Give the extent of all Plasmodium falciparum-infected red blood cells.
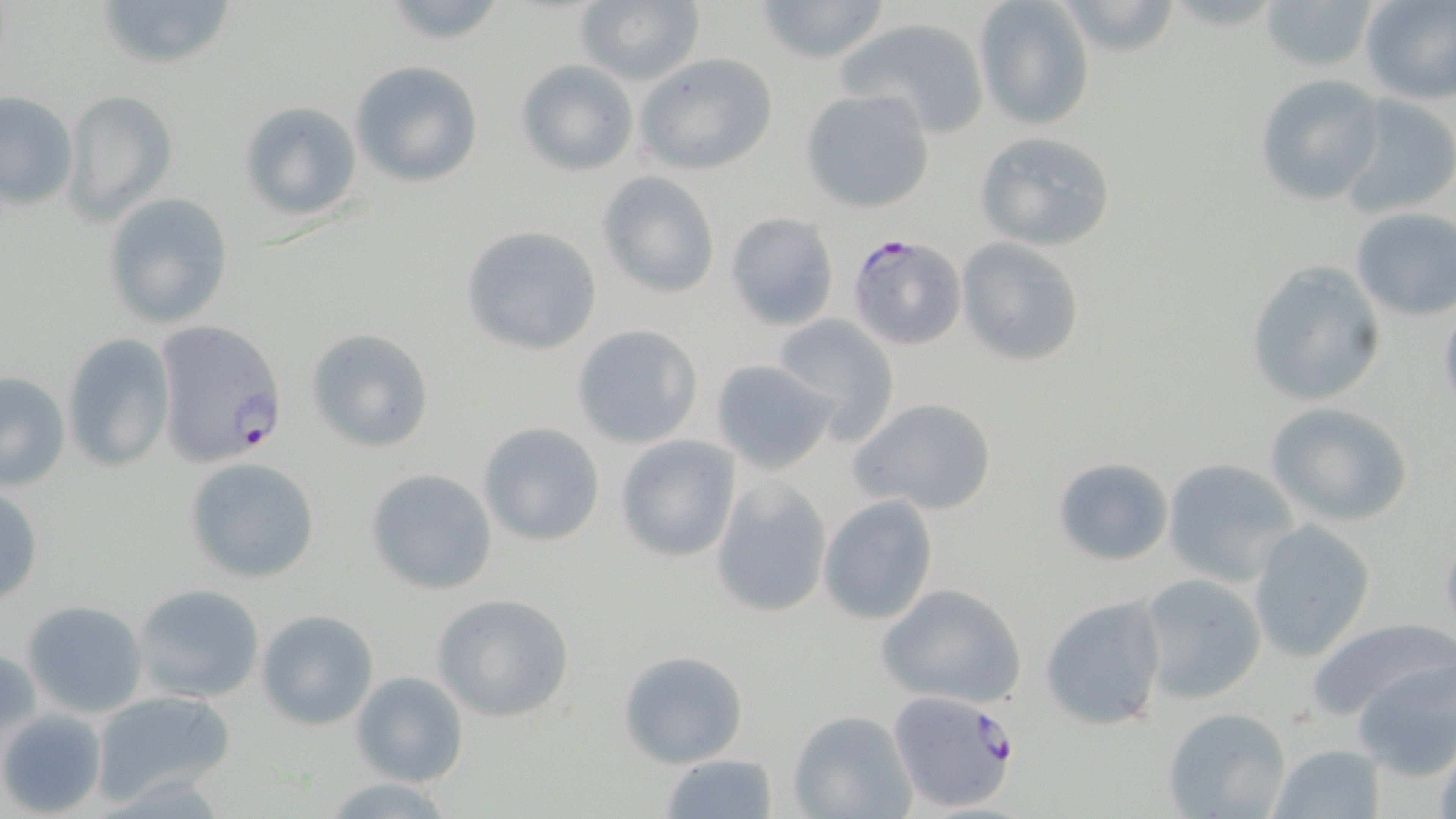
Approximate bounding boxes as named x1/y1/x2/y2 corners in pixels.
Plasmodium falciparum-infected red blood cells: (x1=845, y1=233, x2=967, y2=352), (x1=151, y1=318, x2=288, y2=471), (x1=887, y1=688, x2=1024, y2=815).

slide-level diagnosis = Plasmodium falciparum
field of view = one of a larger specimen
uninfected red blood cell locations = approximate bounding boxes as named x1/y1/x2/y2 corners in pixels: (x1=95, y1=0, x2=237, y2=72), (x1=751, y1=0, x2=892, y2=65), (x1=974, y1=0, x2=1096, y2=130), (x1=1053, y1=0, x2=1187, y2=60), (x1=1258, y1=0, x2=1382, y2=75), (x1=1357, y1=0, x2=1455, y2=104), (x1=377, y1=1, x2=513, y2=48), (x1=572, y1=1, x2=707, y2=87), (x1=836, y1=14, x2=994, y2=139), (x1=633, y1=52, x2=780, y2=176), (x1=514, y1=58, x2=639, y2=176), (x1=351, y1=60, x2=483, y2=188), (x1=1253, y1=74, x2=1385, y2=207), (x1=798, y1=88, x2=936, y2=213), (x1=62, y1=90, x2=177, y2=225), (x1=0, y1=91, x2=79, y2=212), (x1=1337, y1=93, x2=1456, y2=221), (x1=237, y1=100, x2=364, y2=222), (x1=973, y1=129, x2=1119, y2=251), (x1=595, y1=171, x2=721, y2=299), (x1=102, y1=192, x2=235, y2=330), (x1=1350, y1=208, x2=1456, y2=320), (x1=725, y1=211, x2=840, y2=331), (x1=461, y1=225, x2=604, y2=356), (x1=956, y1=237, x2=1087, y2=366), (x1=1243, y1=259, x2=1387, y2=409), (x1=1436, y1=295, x2=1456, y2=419), (x1=773, y1=314, x2=901, y2=443), (x1=571, y1=323, x2=702, y2=449), (x1=306, y1=327, x2=437, y2=454), (x1=62, y1=331, x2=175, y2=472), (x1=709, y1=358, x2=839, y2=475), (x1=0, y1=371, x2=71, y2=492), (x1=850, y1=397, x2=999, y2=517), (x1=1263, y1=401, x2=1412, y2=528), (x1=476, y1=421, x2=607, y2=547), (x1=615, y1=435, x2=741, y2=564), (x1=183, y1=456, x2=323, y2=584), (x1=1050, y1=456, x2=1175, y2=566), (x1=1161, y1=457, x2=1302, y2=586), (x1=364, y1=467, x2=498, y2=596), (x1=710, y1=474, x2=834, y2=619), (x1=0, y1=485, x2=45, y2=607), (x1=817, y1=494, x2=939, y2=626), (x1=1245, y1=522, x2=1375, y2=662), (x1=1438, y1=523, x2=1456, y2=649), (x1=1136, y1=572, x2=1269, y2=703), (x1=876, y1=582, x2=1029, y2=708), (x1=132, y1=583, x2=265, y2=704), (x1=430, y1=593, x2=575, y2=723), (x1=1039, y1=594, x2=1169, y2=732), (x1=23, y1=600, x2=149, y2=717), (x1=256, y1=609, x2=380, y2=731), (x1=1302, y1=616, x2=1456, y2=726), (x1=1, y1=646, x2=40, y2=754), (x1=618, y1=648, x2=748, y2=768), (x1=1352, y1=655, x2=1456, y2=779), (x1=350, y1=670, x2=470, y2=787), (x1=93, y1=690, x2=236, y2=806), (x1=0, y1=707, x2=107, y2=817), (x1=1163, y1=707, x2=1294, y2=819), (x1=790, y1=710, x2=917, y2=818), (x1=1268, y1=743, x2=1387, y2=819), (x1=659, y1=754, x2=779, y2=818), (x1=321, y1=776, x2=456, y2=817)
modality = light microscopy
stain = May-Grünwald-Giemsa
image size = 1456×819 pixels
magnification = 1000x
preparation = thin blood smear